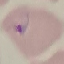

{
  "result": "malaria parasites detected",
  "capture": "smartphone through the microscope eyepiece",
  "image_type": "cell patch, automatically extracted from a larger field of view and resized to 64 × 64 pixels",
  "stain": "Giemsa",
  "preparation": "thin blood smear"
}